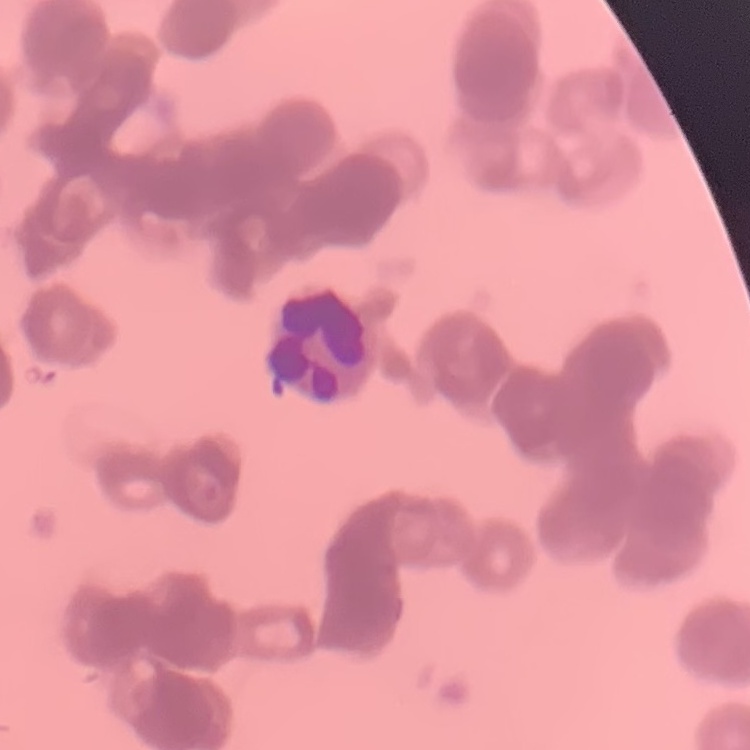
The erythrocytes show rouleaux formation. Square crop of a larger photomicrograph. Thin blood smear. Field's or Giemsa stain.